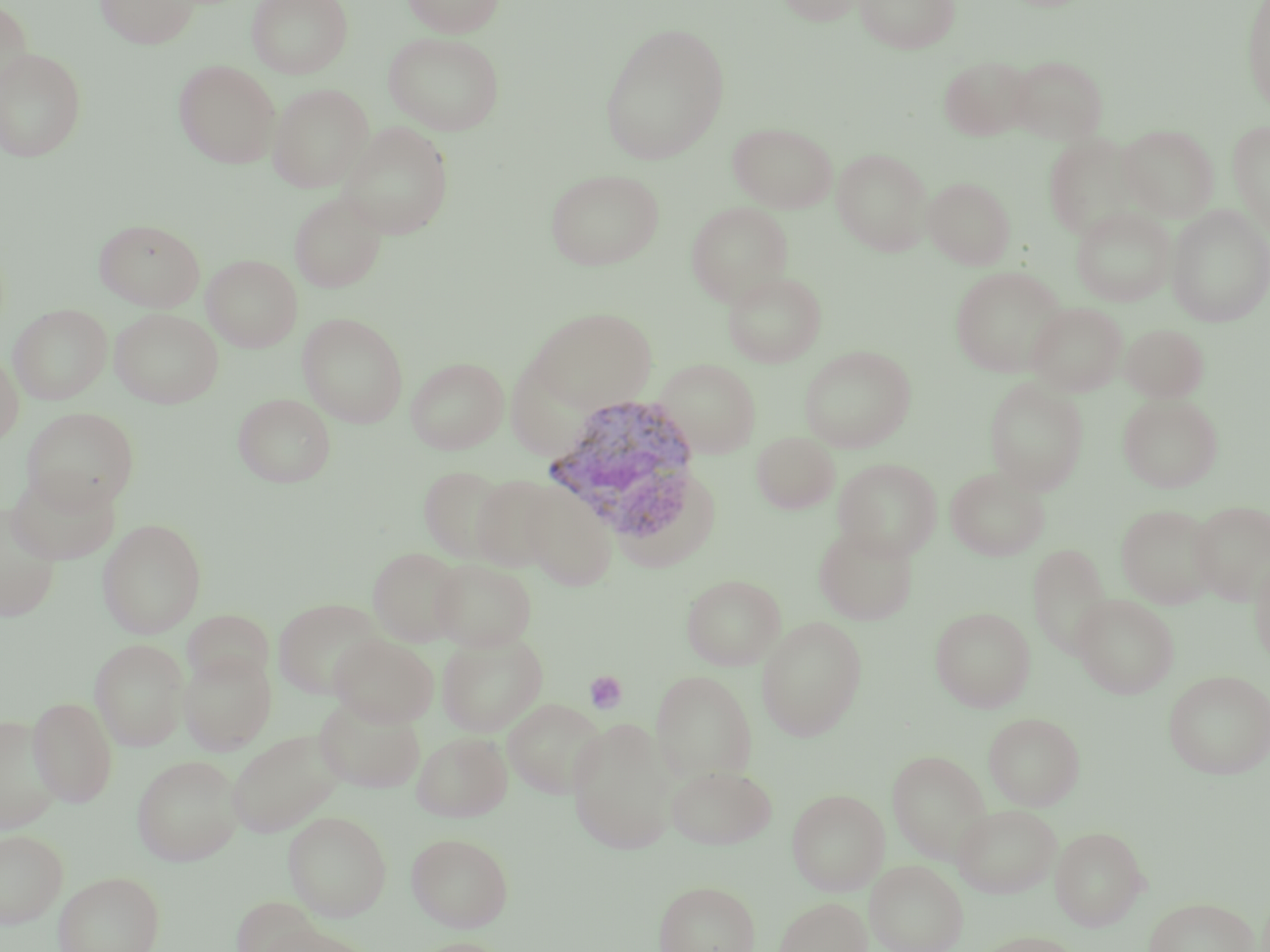
Summary:
  - Coordinate format: approximate bounding boxes as (x1,y1)-(x2,y2) corner pairs in pixels
  - Platelet locations: (584,670)-(627,715)
  - Plasmodium vivax-infected red blood cell locations: (540,394)-(704,531)
  - Uninfected red blood cell locations: (0,0)-(32,95), (95,0)-(199,48), (246,0)-(354,79), (402,0)-(505,36), (773,0)-(871,26), (855,0)-(960,53), (1241,0)-(1270,114), (598,23)-(730,164), (383,31)-(505,135), (0,48)-(87,162), (1009,54)-(1109,144), (939,55)-(1035,141), (174,60)-(281,168), (267,83)-(374,193), (1228,120)-(1269,236), (339,122)-(454,239), (728,122)-(837,213), (1118,124)-(1219,221), (1043,133)-(1146,242), (832,148)-(933,255), (545,168)-(665,270), (923,177)-(1015,269), (289,192)-(388,293), (686,202)-(793,306), (1071,206)-(1176,306), (1166,206)-(1270,327), (94,219)-(206,311), (202,255)-(303,352), (951,266)-(1067,377), (722,270)-(827,367), (1027,302)-(1127,396), (9,304)-(112,403), (110,308)-(223,408), (528,308)-(657,412), (297,312)-(409,427), (1121,323)-(1209,402), (799,346)-(916,452), (0,348)-(23,448), (406,356)-(508,454), (506,356)-(595,461), (656,358)-(761,458), (984,377)-(1088,494), (233,393)-(335,487), (1118,394)-(1223,493), (22,407)-(139,512), (752,432)-(839,514), (834,457)-(942,560), (419,465)-(512,562), (945,467)-(1049,561), (5,469)-(121,565), (471,474)-(563,573), (521,481)-(620,590), (1190,500)-(1270,606), (1116,504)-(1218,608), (0,506)-(61,622), (98,519)-(206,638), (814,525)-(918,625), (1029,544)-(1112,659), (368,547)-(466,645), (1250,549)-(1270,670), (431,558)-(537,652), (681,574)-(786,670), (1073,594)-(1179,698), (273,598)-(385,700), (931,607)-(1035,712), (182,610)-(275,687), (756,616)-(867,741), (436,633)-(548,736), (330,635)-(439,727), (90,638)-(189,749), (178,651)-(276,755), (650,670)-(757,782), (1164,670)-(1270,779), (313,696)-(426,794), (28,697)-(118,806), (503,698)-(606,799), (983,712)-(1085,810), (0,715)-(63,834), (567,719)-(677,855), (226,729)-(345,837), (412,732)-(513,822), (887,750)-(991,862), (132,755)-(243,865), (666,764)-(776,849), (788,789)-(889,895), (952,803)-(1061,898), (283,809)-(392,922), (1050,826)-(1148,930), (0,829)-(68,927), (406,832)-(514,931), (865,860)-(967,952), (53,871)-(164,952), (654,880)-(760,952), (774,896)-(872,952), (233,897)-(335,951), (1144,897)-(1260,952), (255,920)-(375,952), (973,931)-(1083,952), (406,937)-(515,952)
  - Slide-level diagnosis: Plasmodium vivax
  - Preparation: thin blood smear
  - Image size: 1270×952 pixels
  - Modality: optical microscopy
  - Stain: May-Grünwald-Giemsa
  - Magnification: 1000x
  - Field of view: single